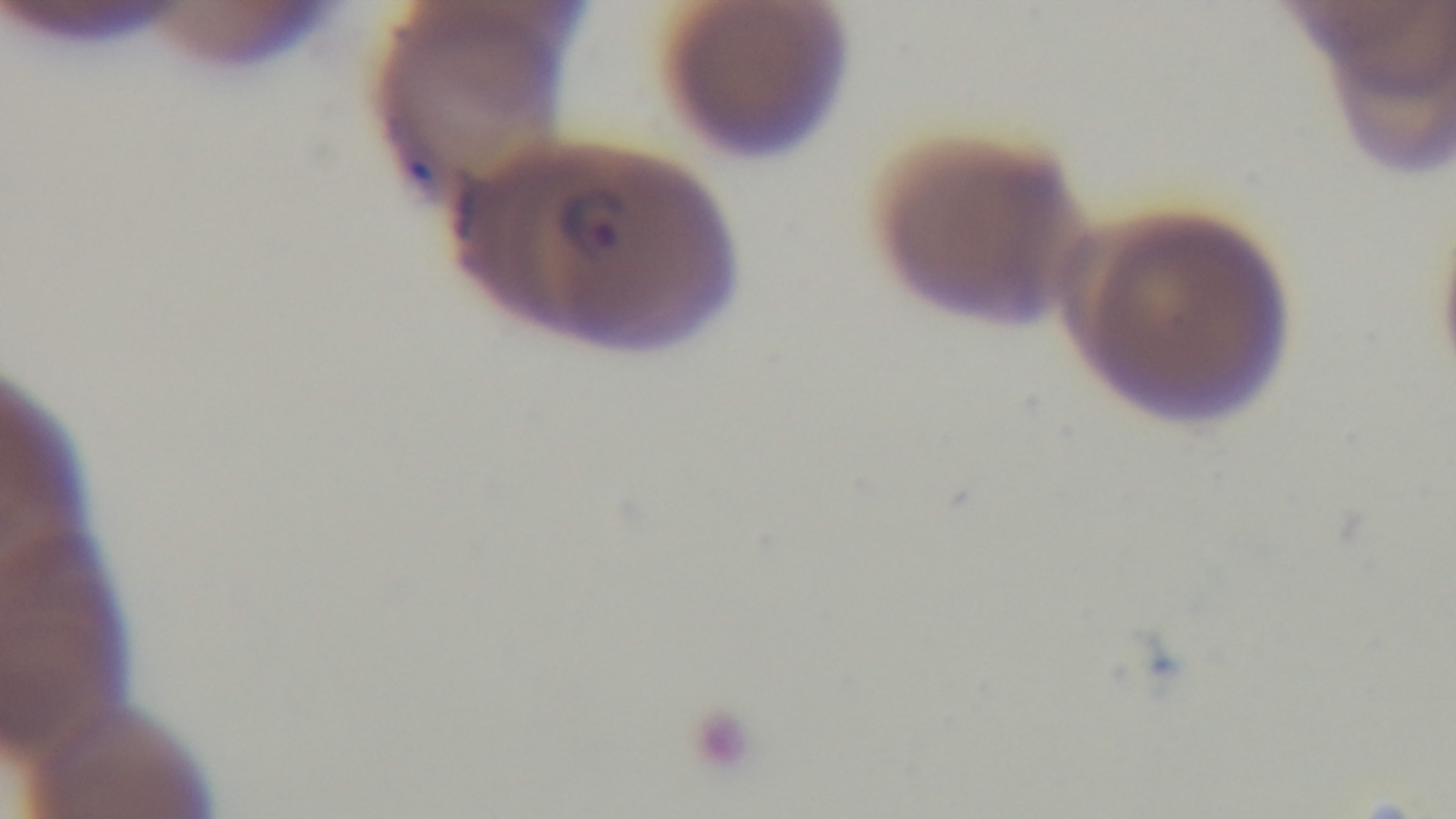
Summary:
  - Stain: Giemsa
  - Capture: mounted 4K digital camera
  - Modality: light microscopy
  - Field of view: single
  - Preparation: thin smear
  - Objective: 100x oil immersion
  - Malaria status: infected